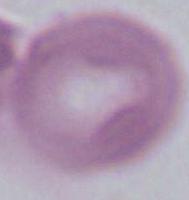
identification = red blood cell
magnification = 1000x
modality = photomicrograph